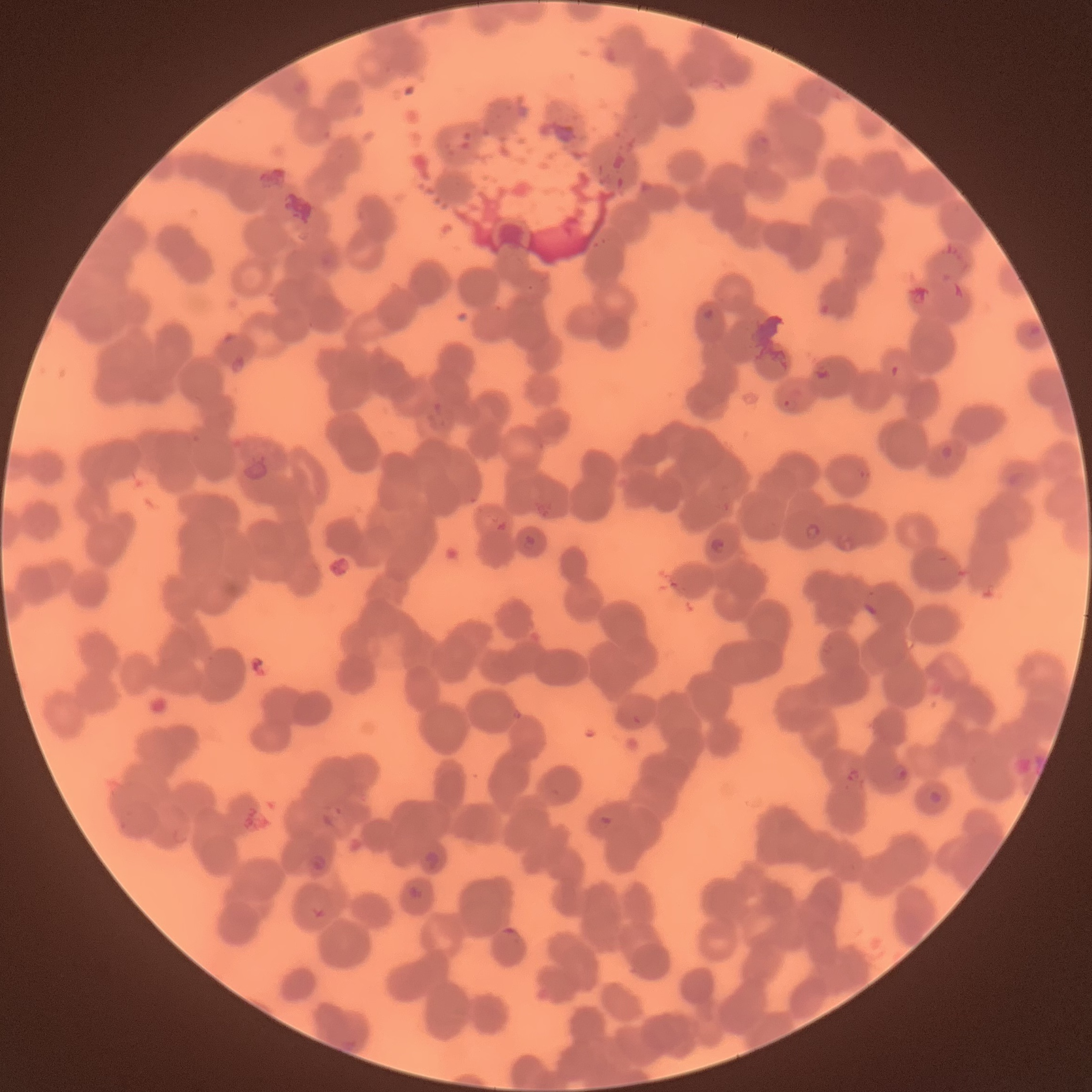

coordinate format = approximate bounding boxes as named x1/y1/x2/y2 corners in pixels
Plasmodium parasite locations = (x1=238, y1=457, x2=269, y2=483), (x1=804, y1=522, x2=821, y2=544), (x1=522, y1=534, x2=536, y2=550), (x1=709, y1=536, x2=726, y2=555), (x1=863, y1=602, x2=880, y2=619), (x1=632, y1=715, x2=641, y2=725), (x1=890, y1=764, x2=908, y2=782), (x1=845, y1=769, x2=860, y2=784), (x1=928, y1=790, x2=942, y2=805), (x1=424, y1=851, x2=441, y2=872), (x1=306, y1=853, x2=327, y2=874), (x1=408, y1=885, x2=426, y2=902), (x1=309, y1=906, x2=328, y2=920), (x1=502, y1=928, x2=526, y2=942)
red blood cell morphology = rouleaux formation
modality = optical microscopy
image size = 1092×1092 pixels
preparation = thin blood smear